Report the malaria status of this cell.
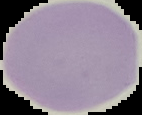

It is uninfected.

Summary:
  - Image type: segmented cell region with the area outside set to black
  - Image size: 142×115 pixels
  - Preparation: thin blood smear